Identify the preparation type.
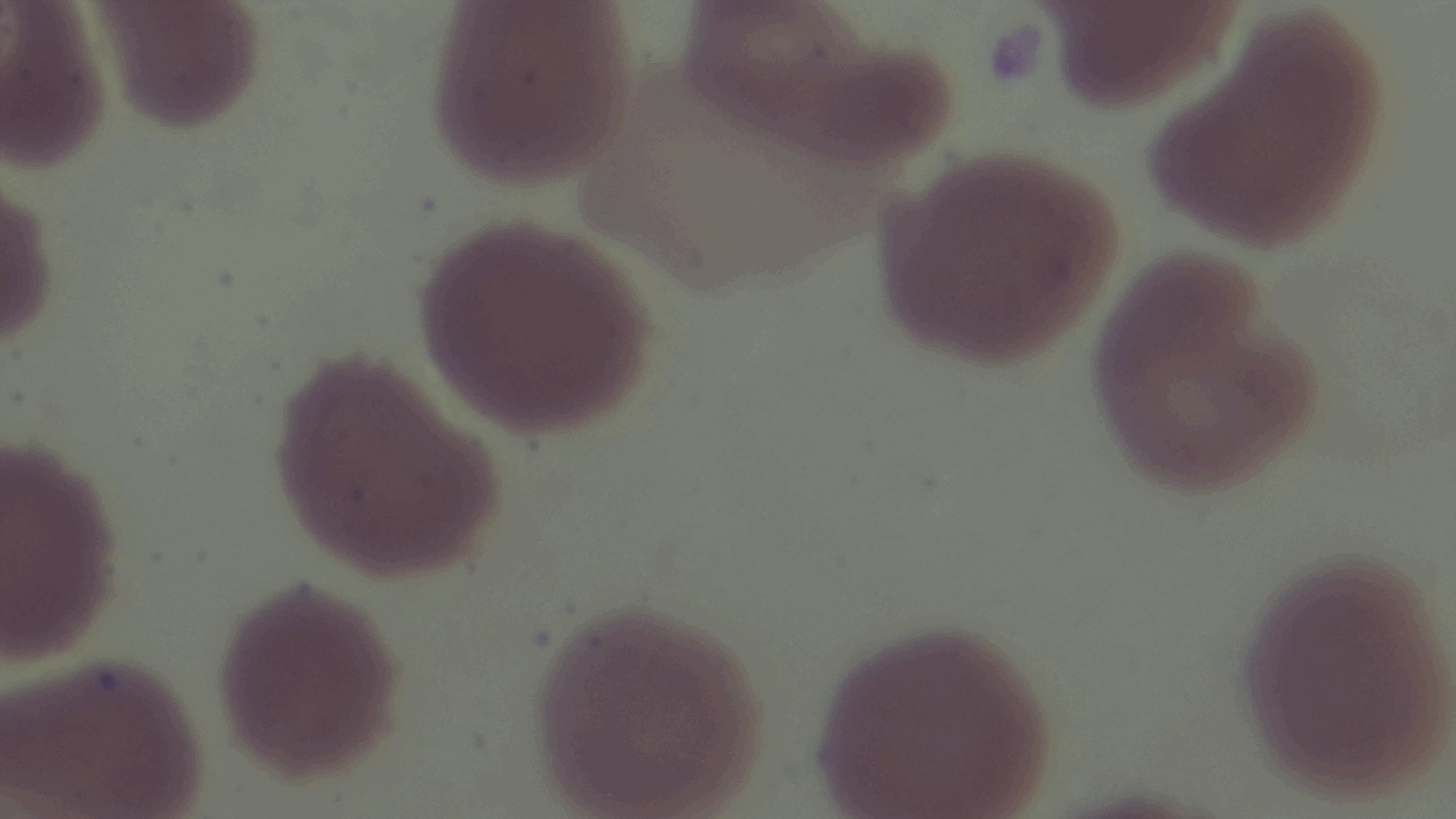
It is a thin blood film.

Light microscopy. Giemsa-stained. Oil-immersion objective, 100x. Malaria status: negative. Single field of view. Mounted 4K digital camera.